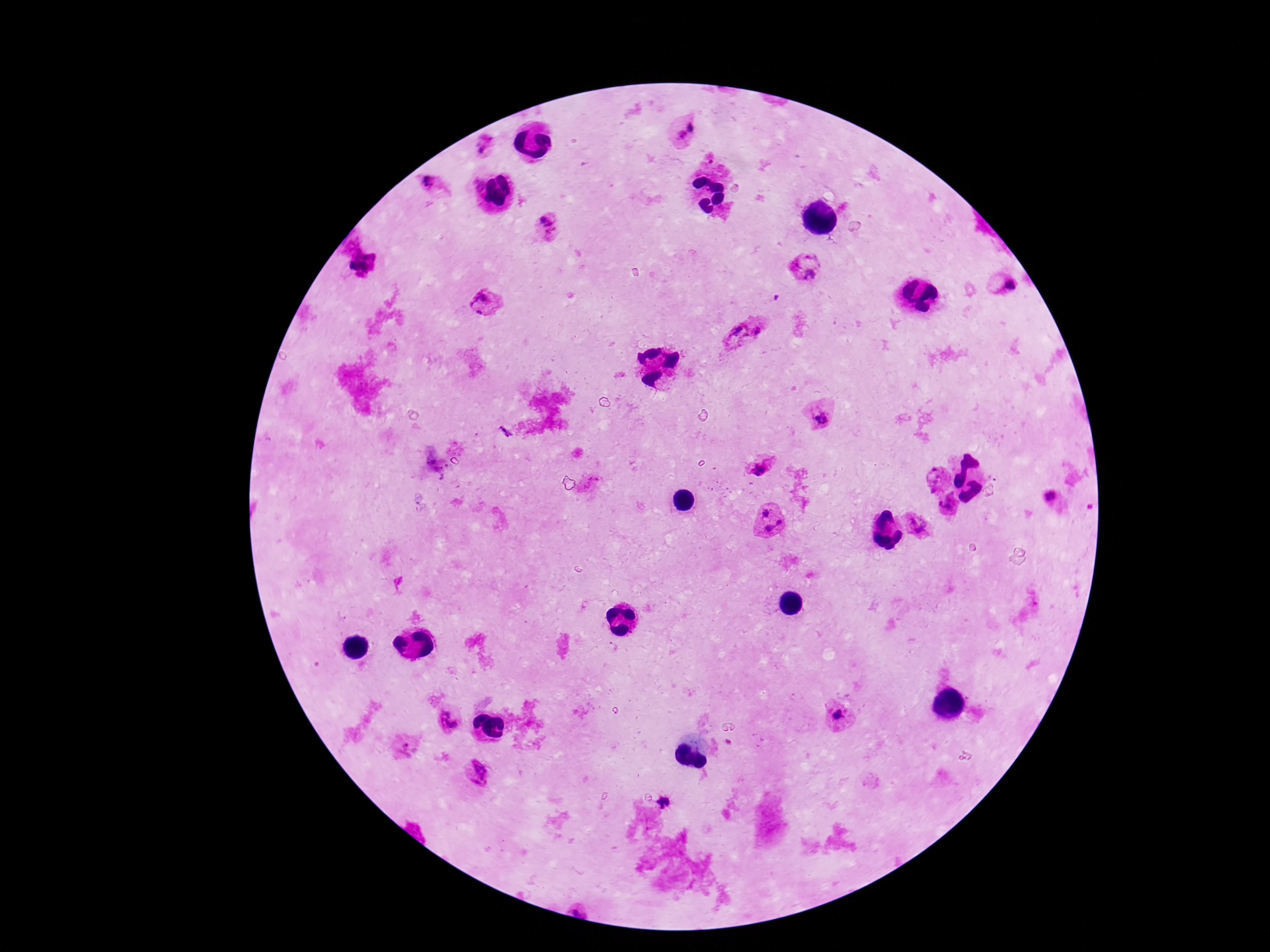
Approximate centers as (x, y) in pixels. Plasmodium parasite locations: (685, 132), (489, 145), (433, 191), (548, 229), (804, 265), (1003, 286), (484, 303), (743, 332), (818, 416), (762, 467), (937, 479), (1052, 497), (950, 505), (766, 511), (780, 524), (917, 525), (768, 529), (838, 715), (452, 719), (406, 745), (477, 772). Thick blood film. Image is 1270×952 pixels. One field from this slide. 100x magnification. Patient malaria status: infected. Smartphone photograph taken through the microscope eyepiece. Giemsa stain.